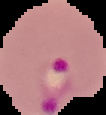

{
  "image_type": "cell region segmented out of the field of view; surrounding area masked to black",
  "preparation": "thin blood smear",
  "malaria_status": "parasitized",
  "image_size": "106×115 pixels"
}